Describe the morphology of the red blood cells.
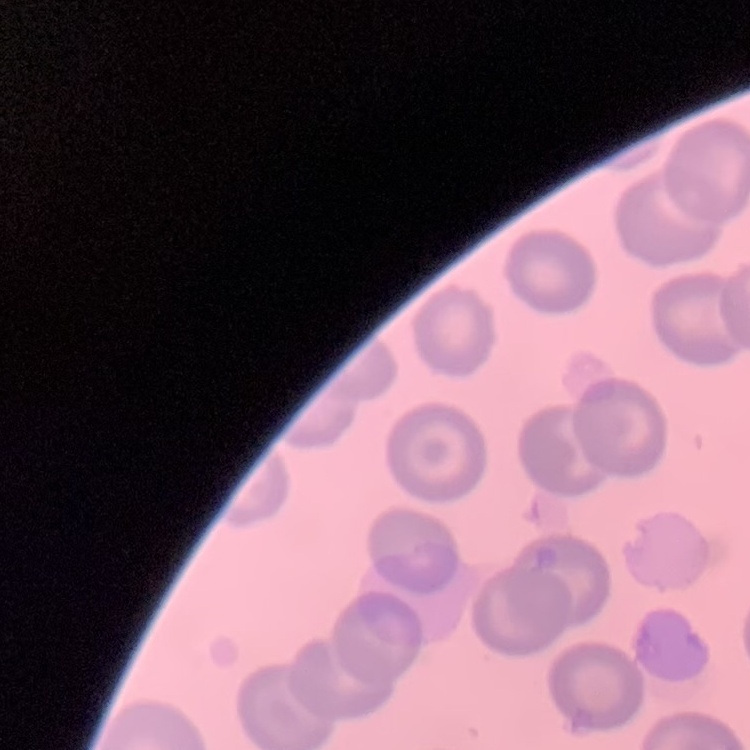

No rouleaux formation.

Field's or Giemsa stain. Square crop of a larger photomicrograph. Thin peripheral smear.